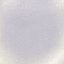

Summary:
  - Result: no malaria parasites seen
  - Image type: cell patch, automatically extracted from a larger field of view and resized to 64 × 64 pixels
  - Capture: smartphone through the microscope eyepiece
  - Stain: Giemsa
  - Preparation: thin blood film